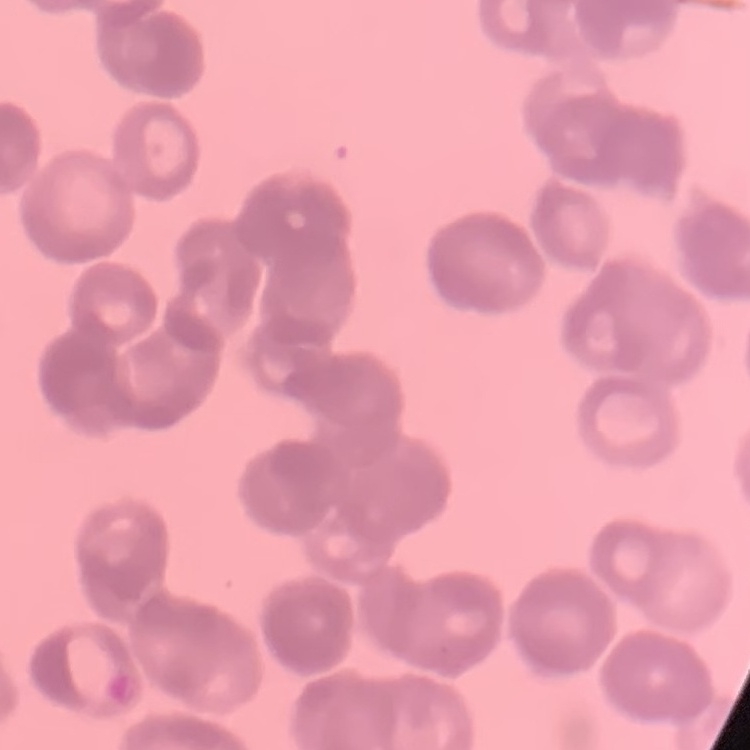
erythrocyte morphology = rouleaux formation
stain = Field's or Giemsa
image type = one tile cut from a larger photomicrograph
preparation = thin peripheral smear